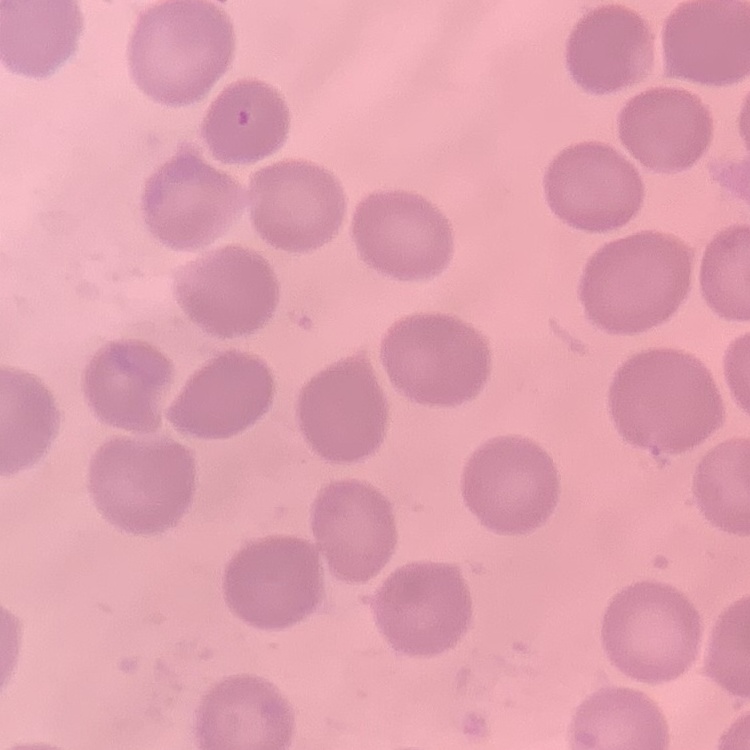

{
  "red_blood_cell_morphology": "no rouleaux formation",
  "stain": "Field's or Giemsa",
  "image_type": "square crop of a larger photomicrograph",
  "preparation": "thin blood film"
}